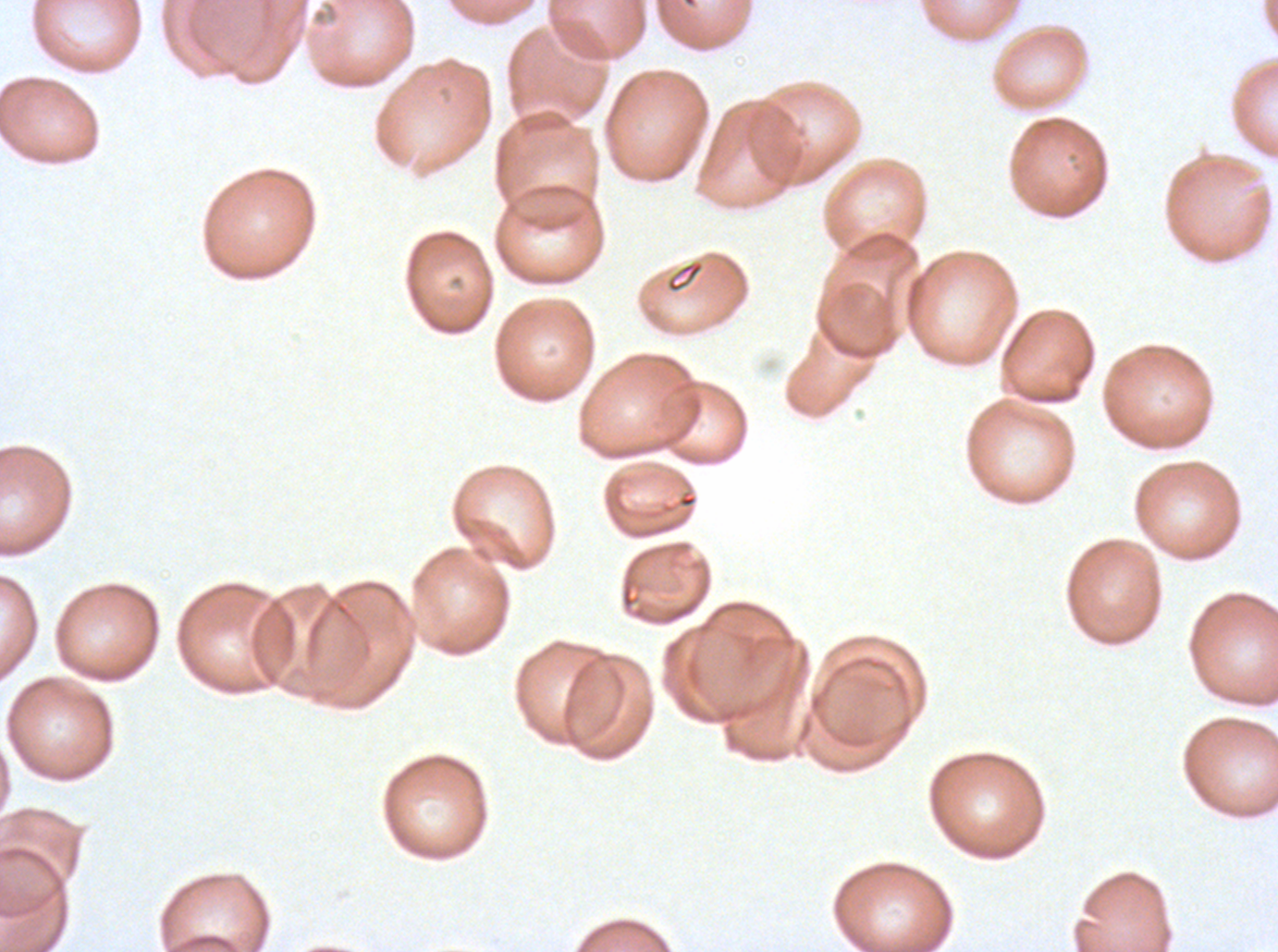
Approximate bounding rectangles given as corner coordinates in pixels from the top-left. Debris locations: (x1=665, y1=258, x2=706, y2=294). One sub-image of a larger composite. Giemsa-stained preparation. Thin blood film. Image is 1278×952 pixels. P. falciparum cultured ex vivo for 24 to 48 hours, from a patient in The Gambia.